Assess this cell for malaria.
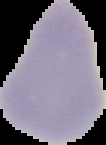
It is uninfected.

image_size: 106×145 pixels
preparation: thin blood smear
image_type: segmented cell region on a black background